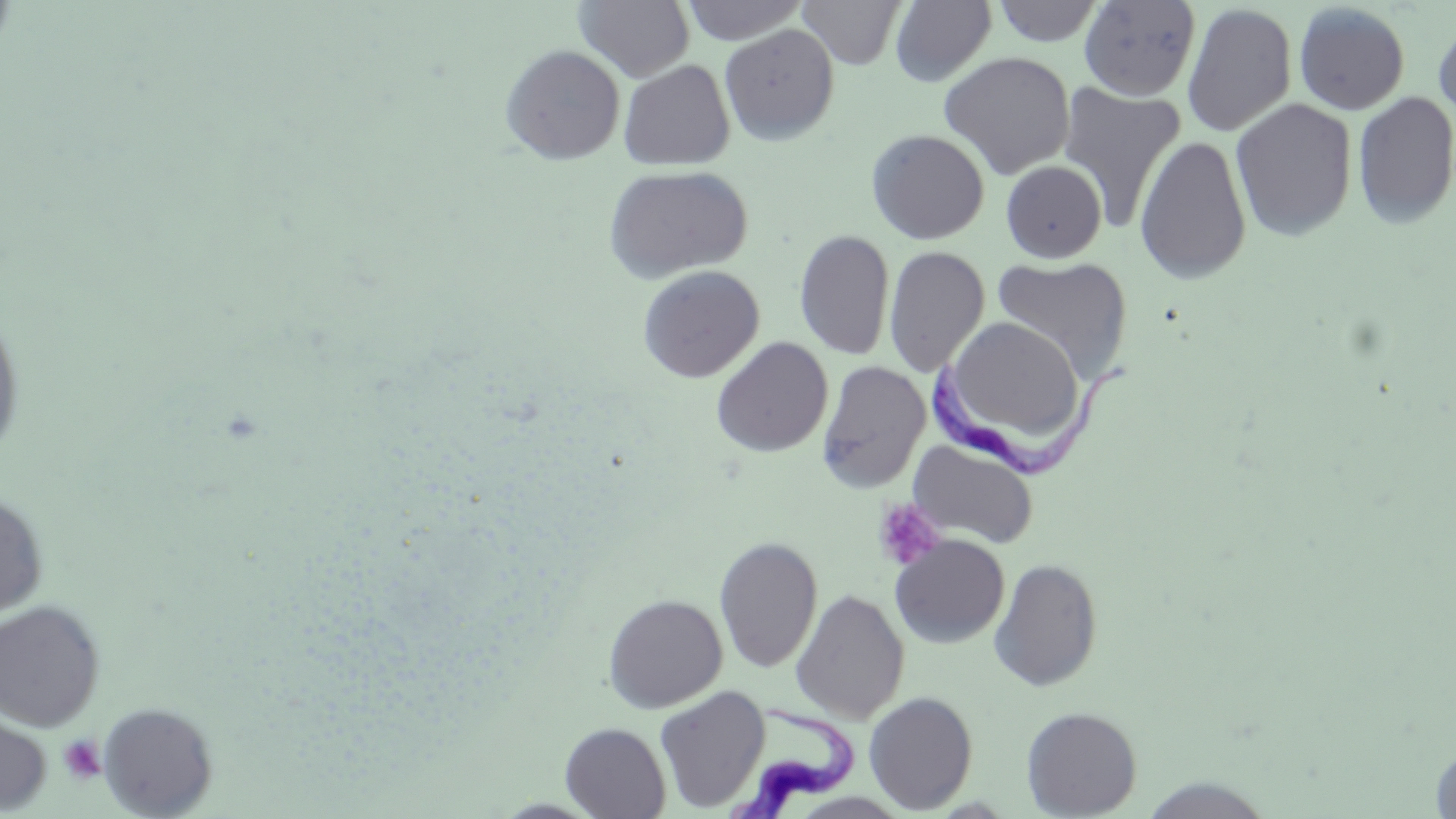
Approximate bounding boxes as [x1, y1, x2, y2] in pixels. Uninfected red blood cell locations: [574, 0, 695, 81], [679, 0, 809, 44], [797, 0, 907, 69], [991, 0, 1105, 47], [888, 1, 996, 85], [1078, 1, 1201, 100], [1182, 3, 1297, 136], [1293, 3, 1410, 115], [1432, 14, 1456, 128], [719, 23, 840, 145], [499, 44, 625, 165], [939, 51, 1075, 180], [618, 60, 736, 171], [1057, 82, 1186, 231], [1352, 90, 1456, 229], [1230, 97, 1358, 242], [866, 128, 990, 245], [1134, 134, 1251, 284], [1001, 161, 1107, 262], [601, 163, 753, 284], [794, 229, 895, 360], [883, 245, 990, 377], [990, 254, 1132, 383], [636, 265, 765, 383], [0, 305, 26, 466], [952, 316, 1090, 439], [711, 336, 833, 458], [816, 359, 931, 493], [908, 439, 1039, 549], [0, 490, 49, 623], [889, 534, 1009, 649], [714, 536, 823, 674], [988, 558, 1104, 692], [790, 589, 910, 724], [603, 593, 728, 713], [0, 599, 106, 731], [654, 685, 771, 812], [864, 691, 978, 813], [97, 701, 219, 818], [1021, 706, 1142, 818], [0, 708, 52, 815], [560, 722, 671, 819], [1429, 740, 1456, 818], [1135, 775, 1276, 818]. Trypanosoma brucei locations: [928, 356, 1135, 484], [729, 700, 864, 817]. Platelet locations: [873, 499, 948, 572], [58, 735, 106, 784]. Slide-level diagnosis: Trypanosoma brucei. 1000x magnification. Image is 1456×819 pixels. Single field of view. May-Grünwald-Giemsa-stained preparation. Thin blood smear. Optical microscopy.